Classify this cell by malaria status.
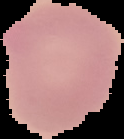
Uninfected.

Image is 124×139 pixels. Segmented cell region on a black background. From a thin blood smear.